Name the blood parasite species.
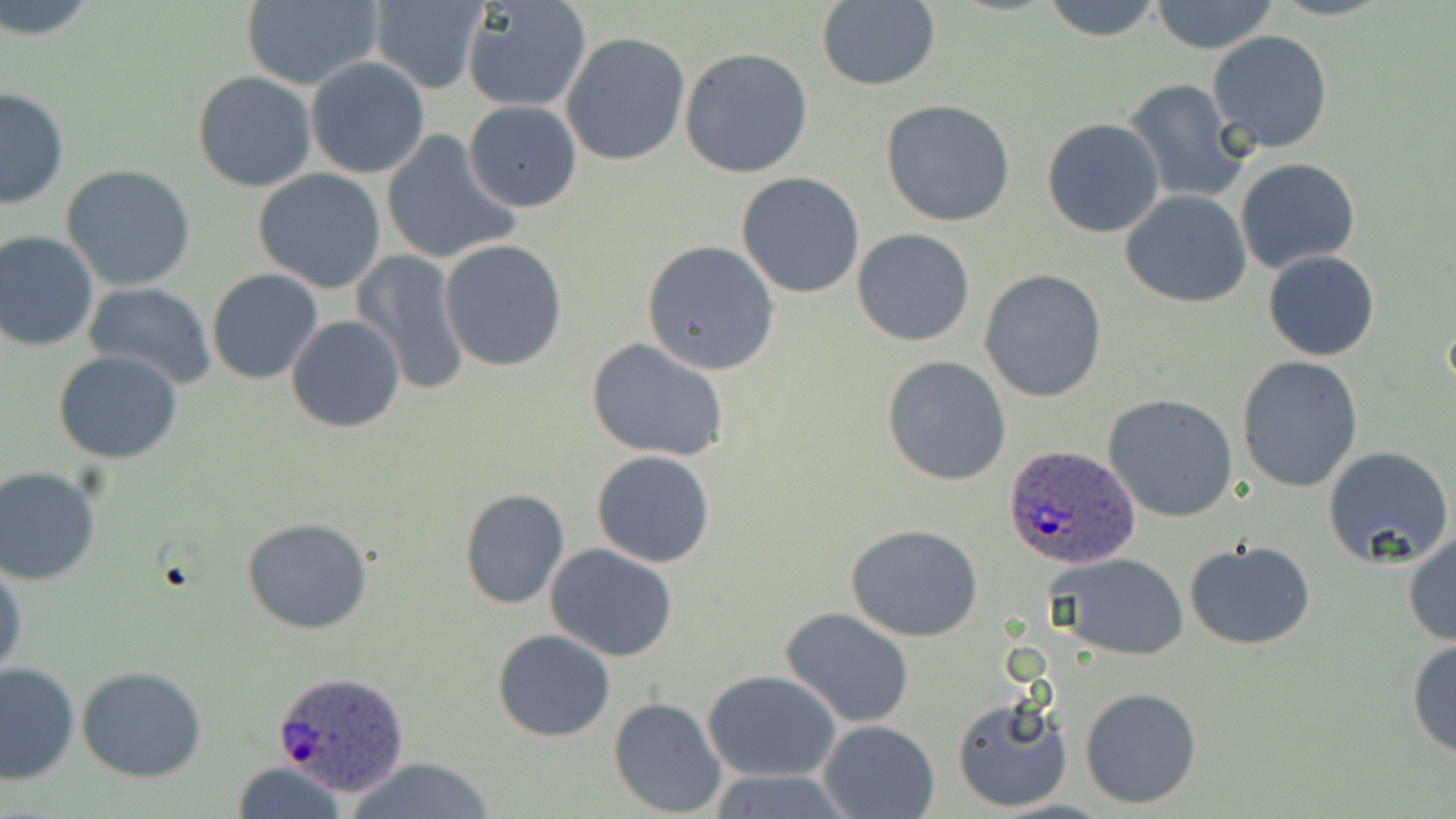
Plasmodium ovale.

Summary:
  - Coordinate format: approximate bounding boxes as (x1,y1)-(x2,y2) corner pairs in pixels
  - Plasmodium ovale-infected red blood cell locations: (1004,441)-(1143,571), (274,670)-(409,795)
  - Uninfected red blood cell locations: (1,0)-(100,40), (814,0)-(941,91), (1040,0)-(1165,43), (1148,0)-(1279,54), (240,1)-(384,90), (367,1)-(488,93), (462,2)-(591,114), (1207,31)-(1333,154), (561,32)-(690,166), (680,46)-(815,178), (305,56)-(430,178), (191,72)-(318,193), (1120,79)-(1252,204), (0,87)-(70,208), (881,99)-(1017,227), (465,100)-(582,211), (1041,118)-(1165,237), (380,129)-(520,267), (1236,158)-(1361,273), (61,163)-(196,291), (252,169)-(386,294), (736,172)-(865,298), (1121,190)-(1252,308), (852,228)-(976,346), (0,230)-(100,352), (641,238)-(780,376), (439,239)-(568,371), (353,248)-(472,394), (1263,250)-(1380,362), (207,268)-(323,383), (978,269)-(1108,403), (83,281)-(219,389), (286,315)-(406,432), (586,338)-(732,463), (53,350)-(184,462), (881,355)-(1011,486), (1236,356)-(1364,492), (1104,392)-(1240,522), (1323,446)-(1455,571), (591,451)-(716,568), (0,465)-(102,585), (458,488)-(570,609), (242,516)-(373,634), (846,524)-(985,642), (1403,531)-(1456,647), (1184,541)-(1316,651), (545,544)-(679,662), (1048,553)-(1191,658), (1,557)-(26,679), (778,607)-(917,730), (494,630)-(615,742), (1407,636)-(1456,760), (0,662)-(81,786), (77,665)-(208,782), (704,670)-(841,781), (1081,686)-(1202,809), (951,694)-(1072,814), (608,696)-(726,817), (818,719)-(941,818), (348,755)-(498,819), (232,763)-(348,819), (711,771)-(856,817)
  - Magnification: 1000x
  - Stain: May-Grünwald-Giemsa
  - Image size: 1456×819 pixels
  - Modality: optical microscopy
  - Preparation: thin blood smear
  - Field of view: single